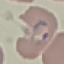

Summary:
  - Result: malaria parasites identified
  - Preparation: thin blood film
  - Image type: automatically extracted cell patch, resized to 64 × 64 pixels
  - Stain: Giemsa
  - Capture: smartphone through the microscope eyepiece